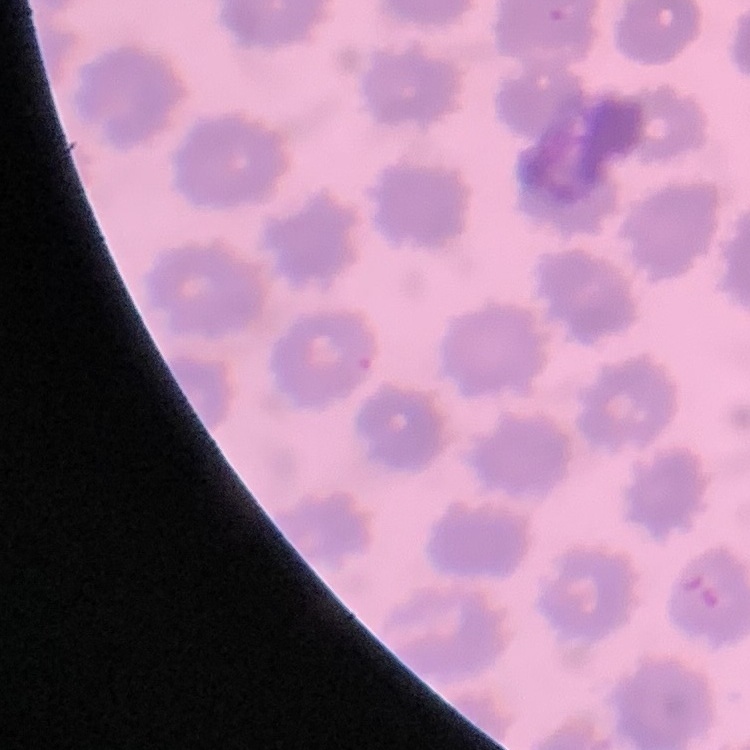
erythrocyte morphology = no rouleaux formation
stain = Field's or Giemsa
image type = one tile cut from a larger photomicrograph
preparation = thin blood smear